Identify the parasite.
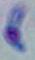
Toxoplasma gondii.

Photomicrograph. 1000x magnification.